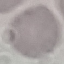
malaria status = uninfected
capture = smartphone through the microscope eyepiece
image type = cell patch, automatically extracted from a larger field of view and resized to 64 × 64 pixels
stain = Giemsa
preparation = thin blood smear